Describe the morphology of the red blood cells.
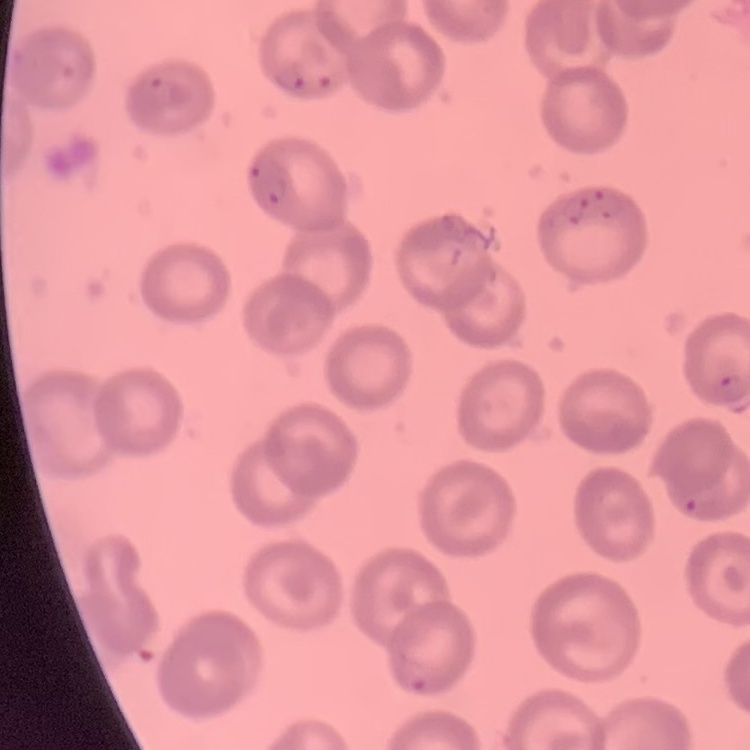

They show no rouleaux formation.

Summary:
  - Preparation: thin blood film
  - Image type: one tile cut from a larger photomicrograph
  - Stain: Field's or Giemsa